Give the position of every malaria parasite.
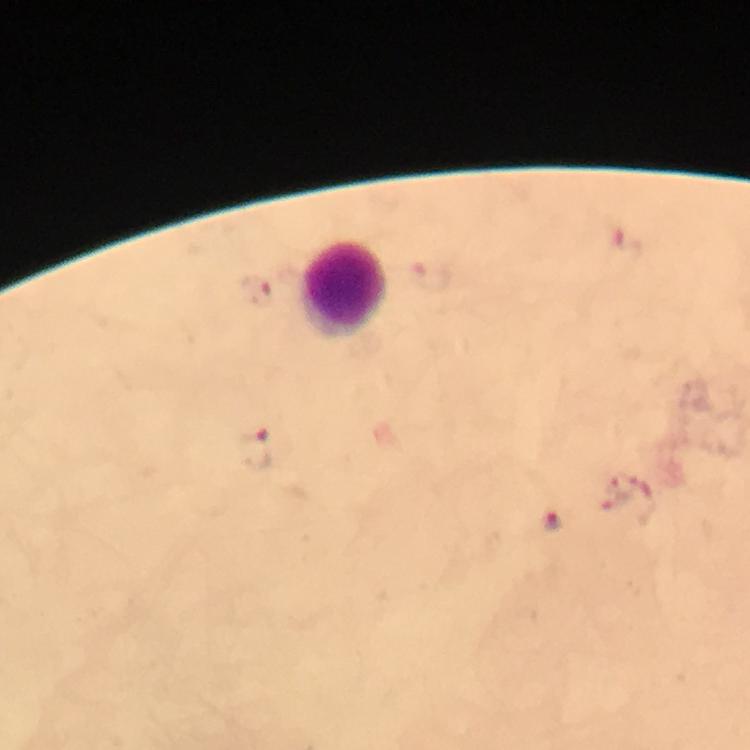

Approximate centers as {x, y} in pixels.
Malaria parasites: {624, 238}, {258, 290}, {256, 449}, {552, 522}.

Leukocyte locations: {346, 289}. Photographed through the microscope with a smartphone camera. From a diagnostic examination for malaria. Giemsa stain. Cropped region of a single field of view. Immersion oil was used. Thick smear. 100x magnification. Image is 750×750 pixels.